Identify the blood parasite species.
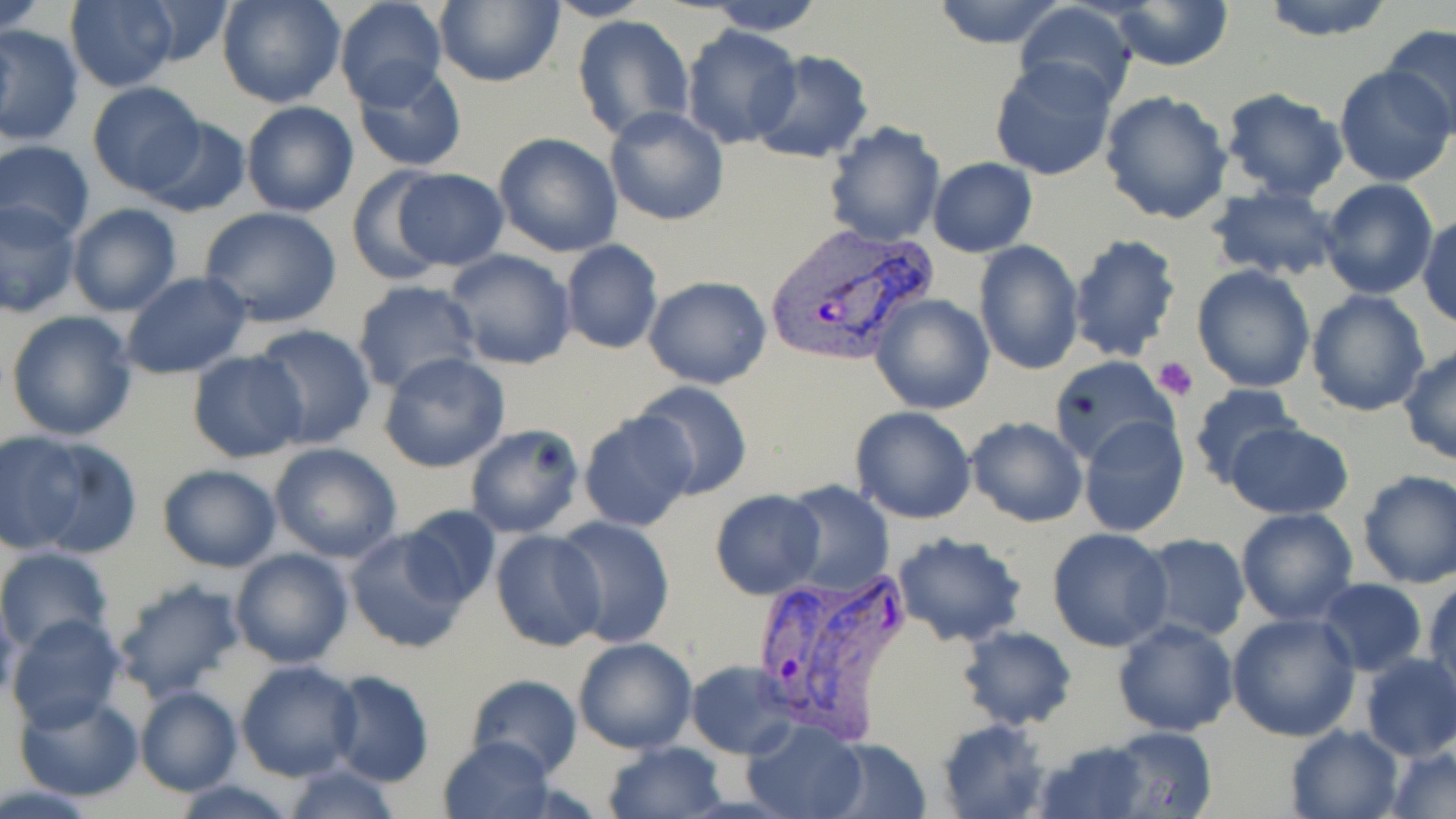

Plasmodium vivax.

Approximate bounding boxes as (x1, y1, x2, y2) in pixels. Plasmodium vivax-infected red blood cell locations: (764, 224, 937, 367), (747, 568, 917, 740). Uninfected red blood cell locations: (1, 0, 49, 34), (64, 0, 180, 91), (130, 0, 236, 69), (333, 0, 448, 108), (433, 0, 564, 87), (542, 0, 651, 22), (702, 0, 827, 35), (930, 0, 1070, 49), (1258, 0, 1397, 41), (216, 1, 345, 108), (1106, 1, 1234, 73), (1015, 2, 1137, 110), (572, 16, 694, 142), (1379, 22, 1456, 138), (1, 26, 84, 146), (680, 26, 802, 149), (748, 50, 874, 165), (990, 60, 1116, 180), (351, 63, 469, 172), (1333, 65, 1456, 187), (87, 82, 205, 197), (1221, 89, 1349, 202), (1097, 90, 1234, 226), (241, 101, 360, 218), (603, 105, 728, 225), (138, 116, 252, 218), (823, 123, 944, 247), (492, 132, 623, 256), (0, 138, 96, 244), (928, 156, 1037, 257), (346, 166, 452, 285), (387, 166, 510, 271), (1318, 179, 1438, 299), (1206, 183, 1343, 281), (0, 199, 82, 318), (67, 203, 183, 315), (199, 205, 343, 327), (1418, 214, 1455, 331), (1066, 233, 1184, 361), (973, 240, 1083, 375), (558, 242, 663, 354), (443, 249, 577, 370), (1191, 264, 1316, 393), (120, 272, 253, 380), (643, 276, 771, 389), (351, 279, 482, 394), (1305, 289, 1432, 417), (870, 294, 995, 415), (5, 309, 140, 442), (250, 324, 377, 450), (1399, 346, 1456, 465), (186, 349, 308, 463), (379, 351, 511, 473), (1049, 356, 1180, 469), (630, 380, 752, 499), (1189, 382, 1306, 491), (850, 406, 977, 524), (578, 409, 700, 533), (965, 415, 1088, 527), (1078, 415, 1188, 538), (1224, 422, 1354, 518), (464, 423, 587, 538), (2, 432, 86, 552), (20, 435, 142, 558), (268, 443, 405, 564), (154, 463, 282, 572), (1356, 470, 1456, 588), (780, 482, 895, 595), (711, 489, 826, 600), (399, 505, 502, 607), (1235, 508, 1360, 625), (552, 515, 676, 647), (344, 526, 470, 655), (1046, 527, 1173, 651), (490, 529, 608, 651), (892, 532, 1028, 648), (1134, 534, 1251, 642), (0, 547, 114, 655), (229, 547, 354, 668), (112, 575, 247, 700), (1425, 575, 1456, 699), (1317, 578, 1428, 675), (1227, 610, 1360, 741), (5, 615, 127, 731), (1113, 619, 1239, 736), (957, 626, 1076, 730), (572, 638, 698, 754), (1356, 653, 1456, 761), (236, 661, 362, 782), (688, 661, 799, 758), (323, 672, 434, 787), (465, 674, 581, 778), (134, 686, 243, 797), (13, 689, 145, 803), (936, 717, 1050, 818), (741, 718, 869, 819), (1284, 724, 1405, 819), (1102, 726, 1220, 818), (439, 734, 556, 816), (820, 736, 932, 819), (1031, 738, 1155, 819), (604, 740, 728, 819), (1385, 743, 1456, 818), (280, 763, 401, 819), (168, 779, 304, 818). Platelet locations: (1152, 356, 1199, 401). One field of a larger specimen. Captured at 1000x magnification. Image is 1456×819 pixels. Thin blood film. Optical microscopy. May-Grünwald-Giemsa-stained preparation.